State which cell type is depicted.
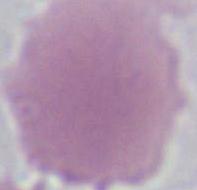

This is an erythrocyte.

Summary:
  - Magnification: 1000x
  - Modality: photomicrograph